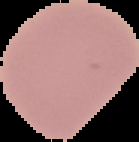

image size = 139×142 pixels
image type = segmented cell region on a black background
preparation = thin blood smear
result = negative for malaria parasites